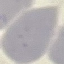
Summary:
  - Result: no malaria parasites detected
  - Image type: automatically extracted cell patch, resized to 64 × 64 pixels
  - Stain: Giemsa
  - Preparation: thin blood smear
  - Capture: smartphone through the microscope eyepiece